Assess the morphology of the erythrocytes.
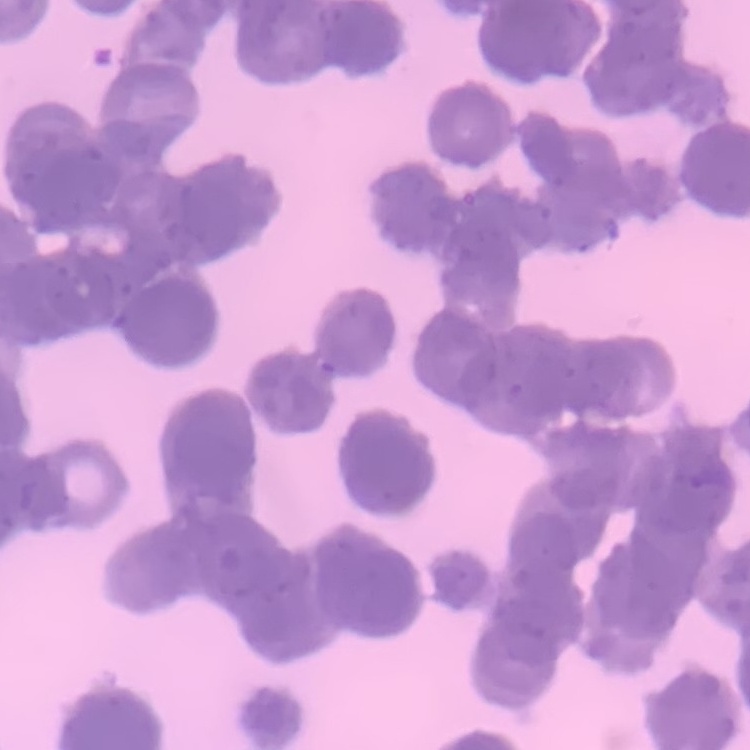

Rouleaux formation.

Thin blood film. Field's or Giemsa stain. Square crop of a larger photomicrograph.